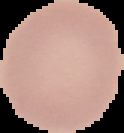
{
  "preparation": "thin blood film",
  "image_type": "segmented cell region on a black background",
  "image_size": "124×133 pixels",
  "result": "negative for Plasmodium parasites"
}